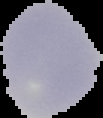 Segmented cell region on a black background. Result: negative for malaria parasites. From a thin blood smear. Image is 103×118 pixels.